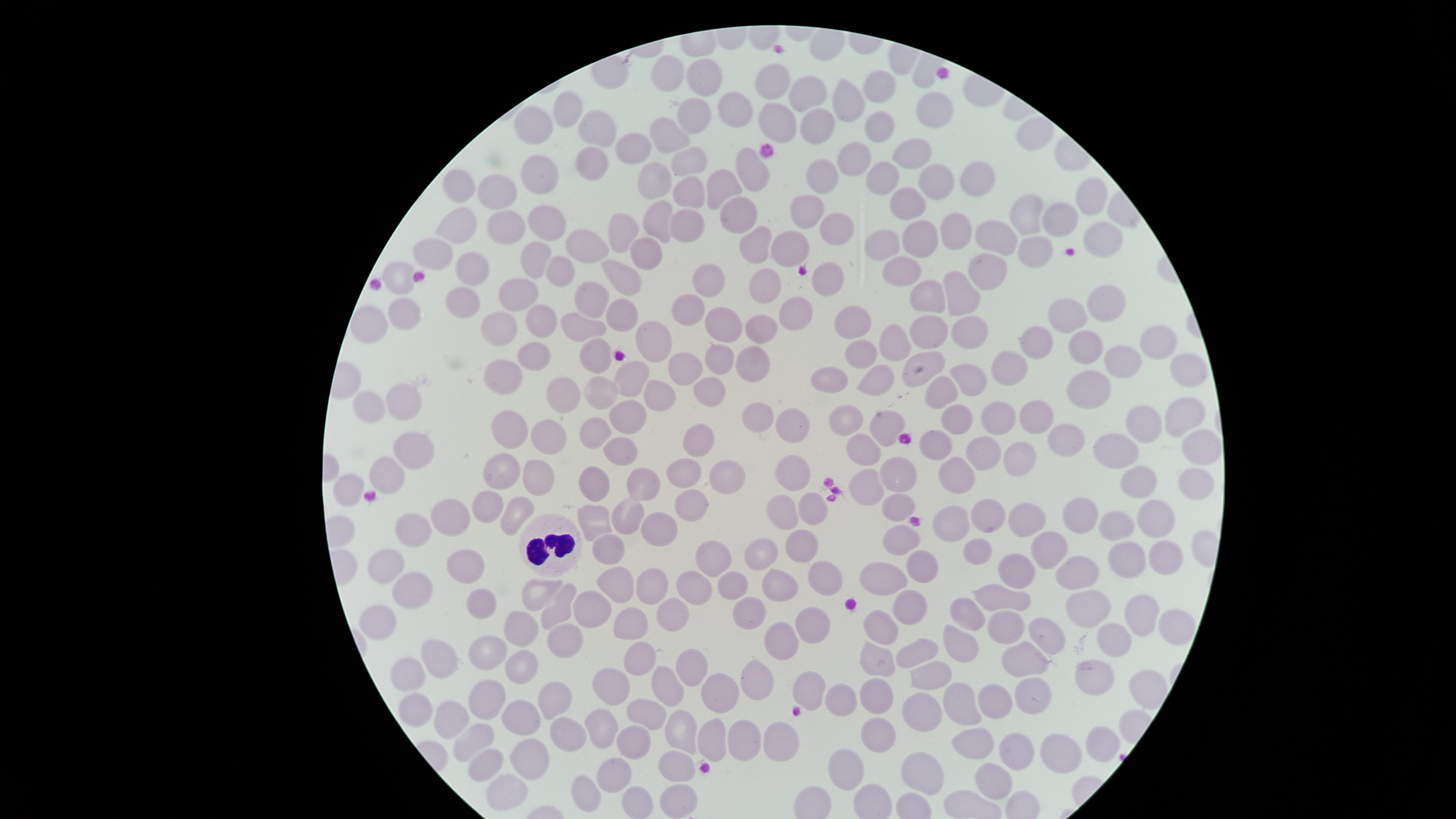

Approximate marker points as (x, y) in pixels.
Summary:
  - White blood cells: (551, 541)
  - Uninfected red blood cells: (672, 74), (699, 77), (776, 82), (878, 90), (809, 96), (852, 102), (934, 108), (737, 110), (566, 112), (693, 115), (775, 120), (527, 122), (878, 127), (605, 129), (669, 132), (813, 133), (636, 147), (911, 152), (689, 158), (595, 160), (852, 161), (752, 169), (540, 170), (975, 174), (883, 175), (814, 177), (654, 179), (937, 179), (724, 180), (501, 186), (455, 189), (686, 195), (1089, 200), (915, 206), (801, 213), (1028, 216), (549, 219), (658, 219), (738, 221), (1068, 221), (454, 223), (621, 226), (689, 227), (836, 227), (505, 230), (957, 230), (1102, 233), (919, 238), (585, 240), (756, 243), (792, 243), (886, 243), (999, 243), (1032, 248), (434, 252), (644, 252), (532, 261), (472, 269), (994, 271), (556, 274), (621, 276), (907, 276), (404, 279), (821, 279), (720, 281), (765, 286), (516, 290), (966, 293), (1104, 296), (457, 299), (929, 300), (590, 301), (687, 311), (621, 313), (799, 315), (407, 317), (715, 320), (1071, 320), (539, 321), (502, 322), (856, 322), (374, 324), (581, 327), (972, 327), (754, 329), (659, 335), (928, 338), (1036, 340), (1152, 341), (899, 343), (1085, 345), (718, 350), (863, 353), (596, 355), (535, 356), (1113, 360), (754, 363), (917, 368), (687, 370), (1010, 372), (1185, 372), (629, 375), (504, 380), (831, 380), (873, 381), (707, 389), (1098, 390), (561, 395), (659, 395), (602, 398), (411, 400), (375, 409), (628, 410), (1180, 416), (1032, 420), (998, 421), (958, 422), (509, 424), (757, 424), (791, 424), (845, 424), (1145, 424), (887, 429), (598, 433), (554, 436), (703, 442), (1198, 442), (1067, 445), (937, 446), (623, 450), (1122, 450), (414, 451), (984, 452), (1018, 453), (865, 456), (388, 470), (530, 470), (497, 471), (793, 472), (683, 473), (727, 473), (896, 474), (957, 474), (644, 477), (1143, 478), (591, 482), (355, 484), (870, 485), (1190, 486), (900, 503), (488, 505), (693, 507), (811, 511), (782, 512), (983, 512), (514, 513), (453, 515), (632, 517), (599, 519), (1082, 519), (1160, 519), (1031, 522), (664, 523), (953, 523), (1121, 526), (419, 529), (898, 539), (801, 542), (611, 546), (1051, 546), (975, 549), (763, 556), (714, 557), (1168, 557), (1127, 560), (466, 561), (922, 562), (394, 566), (1022, 571), (822, 574), (885, 574), (1077, 574), (614, 581), (780, 581), (651, 586), (737, 586), (414, 588), (537, 588), (695, 589), (998, 595), (913, 598), (481, 600), (561, 606), (591, 606), (1086, 609), (750, 613), (1138, 613), (381, 615), (674, 616), (963, 616), (814, 617), (628, 619), (522, 621), (1005, 627), (880, 630), (1164, 631), (563, 636), (1046, 636), (779, 640), (958, 640), (1124, 641), (493, 649), (644, 652), (922, 653), (876, 654), (442, 657), (694, 659), (1025, 659), (526, 663), (1095, 673), (929, 674), (412, 676), (615, 683), (761, 684), (666, 688), (808, 690), (878, 692), (721, 693), (1031, 694), (1140, 696), (552, 697), (486, 698), (841, 702), (921, 702), (996, 703), (418, 707), (646, 708), (964, 708), (457, 713), (522, 715), (598, 722), (565, 732), (676, 732), (884, 732), (474, 734), (747, 736), (713, 737), (628, 742), (782, 742), (978, 744), (1100, 745), (536, 754), (1059, 754), (1014, 756), (488, 759), (676, 762), (851, 767), (612, 768), (930, 773), (507, 785), (988, 788), (592, 792), (679, 799)
  - Preparation: thin smear of blood
  - Field of view: single
  - Presence: no malaria parasites detected
  - Stain: Giemsa
  - Capture: smartphone photograph through the microscope eyepiece
  - Image size: 1456×819 pixels
  - Visible region: circular